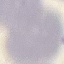
Summary:
  - Result: negative for malaria parasites
  - Capture: smartphone through the microscope eyepiece
  - Preparation: thin smear
  - Stain: Giemsa
  - Image type: automatically extracted cell patch, resized to 64 × 64 pixels